Report the malaria status of this cell.
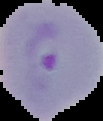
It is parasitized.

image size = 103×121 pixels
preparation = thin blood smear
image type = segmented cell region on a black background